Locate every cell, classifying each as a parasitized RBC, an uninfected RBC, or a WBC.
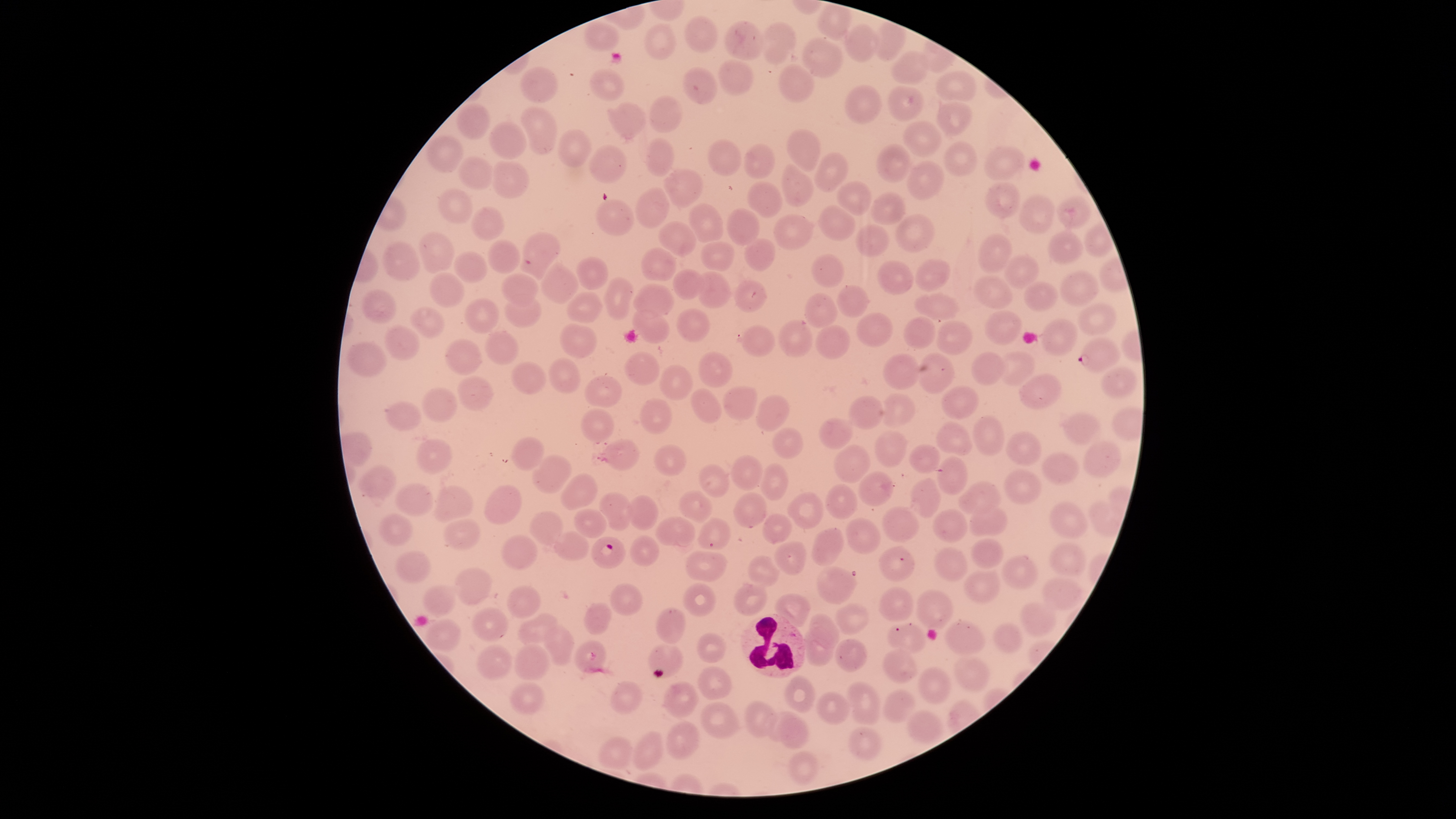
Approximate bounding boxes as [left, top, right, bottom] in pixels.
Parasitized RBCs: [517, 232, 560, 280], [1076, 338, 1121, 372], [592, 536, 626, 568].
Uninfected RBCs: [685, 16, 716, 52], [723, 21, 764, 61], [643, 22, 676, 61], [760, 22, 795, 64], [583, 23, 619, 52], [844, 24, 879, 61], [801, 38, 844, 77], [891, 51, 929, 84], [716, 58, 754, 97], [779, 65, 813, 101], [520, 67, 558, 104], [682, 67, 719, 104], [590, 68, 625, 101], [934, 71, 977, 102], [845, 85, 881, 122], [888, 86, 923, 121], [647, 95, 683, 133], [456, 103, 489, 138], [607, 103, 649, 138], [937, 103, 971, 135], [519, 108, 557, 153], [904, 120, 941, 156], [488, 122, 526, 160], [557, 130, 591, 168], [786, 131, 821, 171], [425, 136, 464, 172], [644, 138, 674, 176], [706, 139, 741, 176], [943, 140, 977, 175], [744, 143, 775, 180], [876, 143, 911, 183], [588, 145, 627, 183], [984, 145, 1027, 181], [813, 153, 848, 193], [458, 156, 493, 191], [489, 160, 529, 199], [781, 162, 815, 207], [906, 162, 945, 199], [663, 168, 703, 209], [836, 180, 871, 215], [748, 182, 782, 218], [984, 182, 1020, 219], [635, 187, 671, 228], [436, 188, 474, 224], [871, 191, 905, 226], [1018, 194, 1056, 233], [1058, 197, 1089, 228], [596, 199, 634, 236], [688, 203, 726, 242], [817, 204, 856, 241], [469, 206, 503, 241], [726, 208, 760, 246], [771, 214, 813, 251], [895, 215, 934, 253], [657, 221, 697, 257], [855, 223, 888, 257], [1046, 231, 1086, 268], [419, 232, 455, 274], [979, 234, 1013, 273], [744, 238, 774, 271], [486, 240, 520, 275], [383, 241, 420, 281], [701, 242, 734, 272], [640, 248, 676, 282], [453, 252, 487, 284], [810, 253, 845, 288], [1005, 255, 1039, 289], [576, 256, 607, 290], [915, 259, 950, 292], [877, 261, 914, 296], [541, 263, 579, 304], [672, 269, 704, 299], [696, 271, 731, 308], [1059, 271, 1098, 307], [501, 273, 541, 306], [429, 274, 464, 307], [971, 275, 1014, 310], [604, 278, 634, 320], [732, 280, 767, 312], [1023, 281, 1058, 313], [632, 284, 674, 318], [837, 285, 868, 318], [360, 290, 397, 323], [567, 291, 603, 324], [804, 292, 837, 328], [912, 292, 959, 322], [503, 293, 541, 329], [461, 298, 499, 334], [1078, 303, 1117, 336], [408, 308, 444, 337], [676, 308, 710, 343], [631, 310, 669, 342], [984, 310, 1022, 344], [854, 313, 894, 346], [903, 317, 936, 349], [778, 320, 813, 357], [1039, 320, 1077, 357], [559, 322, 595, 359], [936, 322, 972, 354], [814, 324, 851, 361], [740, 325, 776, 357], [384, 326, 421, 360], [485, 330, 518, 365], [347, 339, 386, 380], [444, 339, 483, 376], [624, 350, 660, 387], [971, 351, 1006, 386], [698, 352, 733, 387], [999, 352, 1036, 386], [915, 353, 954, 395], [881, 354, 919, 390], [549, 358, 579, 394], [510, 361, 547, 395], [660, 365, 693, 400], [1101, 368, 1135, 400], [1017, 374, 1061, 409], [584, 376, 623, 409], [457, 377, 493, 412], [941, 385, 977, 420], [421, 387, 458, 424], [722, 387, 757, 420], [691, 388, 722, 423], [879, 394, 916, 429], [639, 395, 671, 435], [755, 396, 792, 430], [849, 396, 882, 431], [385, 400, 423, 430], [581, 408, 614, 444], [1063, 413, 1101, 444], [973, 417, 1005, 455], [818, 418, 854, 450], [935, 421, 972, 454], [773, 427, 804, 458], [874, 431, 909, 468], [1006, 431, 1043, 468], [511, 437, 545, 469], [602, 439, 639, 472], [1083, 439, 1120, 478], [416, 440, 452, 476], [832, 442, 871, 481], [653, 444, 686, 477], [909, 445, 941, 473], [1042, 452, 1081, 485], [533, 454, 572, 496], [731, 455, 762, 491], [935, 456, 969, 494], [761, 463, 789, 501], [698, 464, 731, 498], [359, 466, 398, 497], [1002, 469, 1043, 505], [857, 470, 893, 507], [560, 473, 597, 511], [910, 478, 942, 516], [958, 481, 1002, 517], [824, 483, 858, 519], [396, 484, 434, 516], [482, 485, 522, 525], [433, 486, 473, 522], [678, 491, 714, 524], [732, 491, 769, 529], [788, 491, 824, 528], [599, 493, 633, 532], [627, 494, 659, 530], [1049, 500, 1088, 538], [1087, 500, 1123, 537], [881, 506, 919, 544], [968, 506, 1009, 538], [574, 508, 607, 538], [932, 508, 967, 544], [528, 510, 565, 548], [379, 513, 412, 546], [761, 513, 792, 543], [655, 517, 696, 549], [697, 518, 729, 551], [845, 518, 881, 553], [443, 519, 479, 550], [811, 529, 845, 566], [553, 531, 589, 561], [501, 535, 537, 569], [629, 535, 660, 568], [970, 538, 1005, 570], [774, 541, 807, 574], [1048, 542, 1087, 578], [879, 547, 915, 582], [934, 548, 969, 582], [395, 550, 432, 583], [685, 551, 729, 581], [748, 555, 781, 587], [1002, 555, 1039, 590], [814, 566, 859, 605], [455, 568, 494, 606], [963, 569, 999, 605], [1041, 576, 1083, 612], [733, 582, 768, 616], [610, 583, 643, 617], [423, 584, 457, 616], [683, 584, 717, 618], [506, 585, 542, 619], [879, 587, 915, 622], [916, 590, 955, 628], [775, 593, 811, 627], [584, 602, 612, 636], [1019, 602, 1056, 634], [836, 603, 869, 634], [471, 607, 510, 641], [656, 607, 686, 643], [810, 613, 840, 649], [517, 614, 559, 647], [428, 619, 462, 653], [944, 620, 985, 654], [992, 623, 1023, 654], [543, 624, 573, 666], [887, 624, 928, 654], [804, 625, 834, 666], [698, 630, 727, 663], [836, 639, 867, 672], [574, 641, 607, 674], [515, 643, 550, 679], [647, 643, 684, 678], [477, 644, 512, 679], [883, 649, 919, 683], [950, 656, 990, 691], [698, 665, 730, 698], [917, 666, 951, 705], [783, 674, 815, 712], [845, 680, 880, 725], [611, 681, 642, 712], [665, 681, 696, 717], [509, 682, 544, 716], [882, 690, 919, 725], [817, 691, 852, 724], [699, 702, 740, 739], [743, 702, 777, 737], [905, 710, 943, 741], [763, 711, 803, 741], [778, 716, 812, 747], [664, 722, 700, 761], [847, 727, 879, 759], [634, 734, 662, 770], [599, 737, 634, 769], [787, 751, 818, 784].
WBCs: [740, 614, 805, 678].

Image is 1456×819 pixels. Photographed with a smartphone camera through the microscope eyepiece. Circular visible region. Giemsa-stained preparation. Species: Plasmodium falciparum. One field of view of the specimen. Thin smear of blood.